Classify this cell by malaria status.
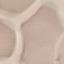

It is uninfected.

preparation = thin blood smear
stain = Giemsa
image type = cell patch, automatically extracted from a larger field of view and resized to 64 × 64 pixels
capture = smartphone camera at the microscope eyepiece